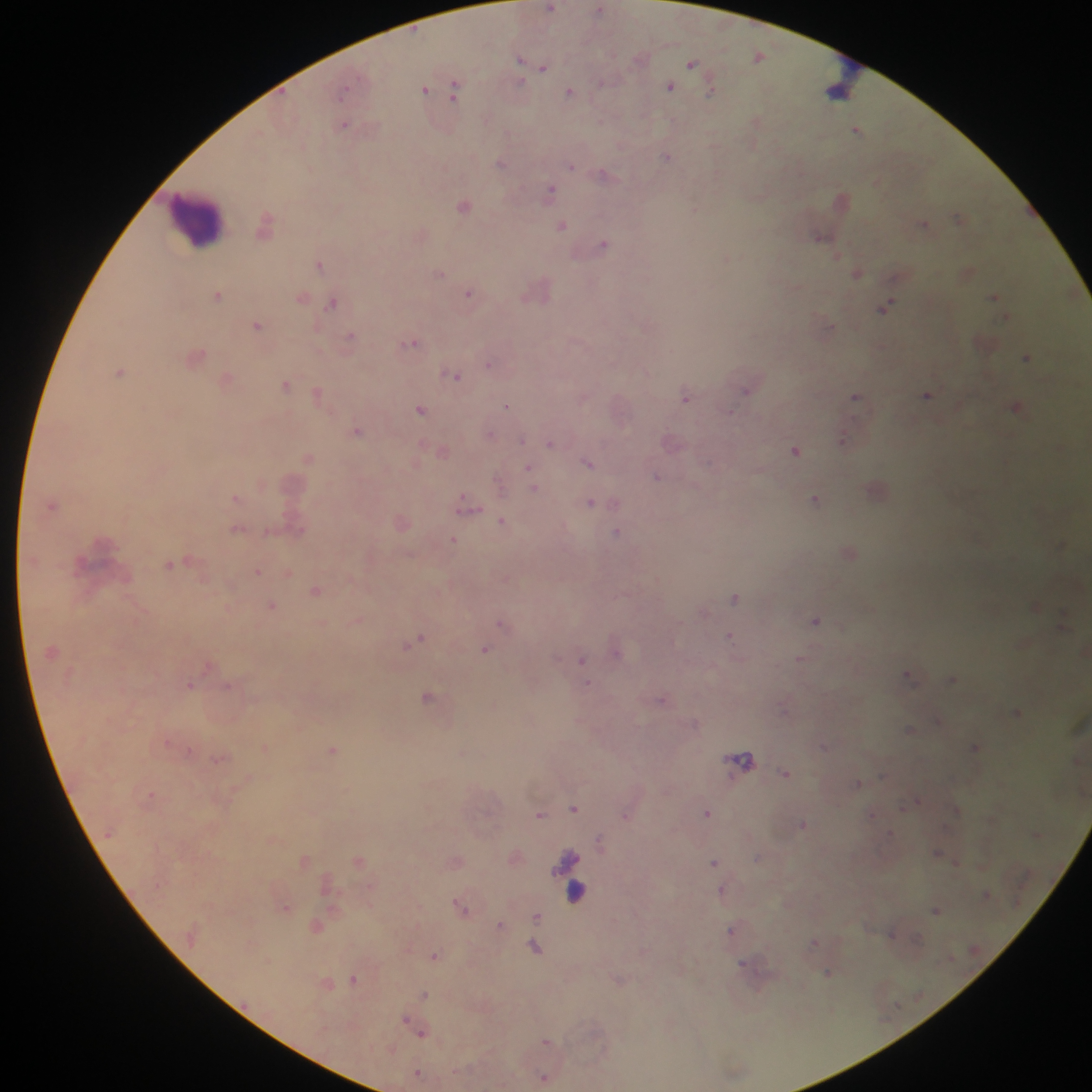
leukocyte locations = approximate centers as {x, y} in pixels: {847, 76}, {196, 222}, {583, 899}
image size = 1092×1092 pixels
field of view = single
Plasmodium parasite locations = approximate centers as {x, y} in pixels: {552, 8}, {758, 57}, {521, 58}, {692, 63}, {543, 69}, {520, 82}, {456, 86}, {671, 86}, {425, 89}, {712, 91}, {569, 93}, {602, 120}, {757, 122}, {344, 126}, {856, 131}, {668, 157}, {501, 164}, {571, 167}, {312, 172}, {604, 175}, {552, 192}, {844, 196}, {465, 207}, {695, 209}, {957, 216}, {267, 217}, {924, 223}, {562, 226}, {821, 236}, {604, 244}, {838, 255}, {727, 257}, {320, 264}, {857, 273}, {440, 274}, {469, 293}, {218, 295}, {302, 295}, {994, 296}, {332, 305}, {886, 306}, {256, 325}, {350, 338}, {414, 344}, {1027, 358}, {488, 364}, {120, 372}, {457, 376}, {285, 385}, {746, 389}, {317, 393}, {926, 395}, {857, 396}, {686, 399}, {508, 405}, {1015, 408}, {420, 411}, {358, 430}, {849, 431}, {522, 441}, {550, 444}, {423, 445}, {796, 451}, {589, 463}, {528, 467}, {656, 474}, {499, 486}, {535, 488}, {237, 499}, {815, 499}, {591, 501}, {50, 505}, {463, 508}, {502, 521}, {618, 532}, {454, 539}, {1058, 544}, {170, 565}, {258, 571}, {288, 571}, {317, 591}, {734, 599}, {272, 606}, {142, 611}, {357, 620}, {817, 620}, {501, 624}, {421, 636}, {730, 636}, {414, 641}, {407, 646}, {486, 648}, {799, 658}, {582, 659}, {209, 665}, {909, 675}, {952, 679}, {587, 683}, {230, 685}, {190, 686}, {428, 696}, {663, 700}, {938, 719}, {909, 729}, {168, 741}, {823, 745}, {976, 745}, {264, 747}, {333, 749}, {190, 750}, {218, 758}, {744, 762}, {787, 773}, {858, 782}, {152, 795}, {155, 795}, {919, 800}, {574, 809}, {957, 810}, {707, 813}, {872, 813}, {540, 814}, {626, 815}, {803, 823}, {599, 842}, {937, 852}, {305, 859}, {358, 860}, {715, 863}, {955, 863}, {720, 889}, {457, 903}, {286, 907}, {464, 908}, {935, 909}, {537, 917}, {500, 924}, {731, 931}, {891, 934}, {813, 942}, {535, 947}, {433, 955}, {269, 961}, {742, 962}, {827, 972}, {354, 978}, {425, 993}, {404, 1018}, {422, 1034}, {547, 1040}, {418, 1072}, {544, 1075}
country = Ghana
capture = mobile-phone photograph through a microscope
preparation = thick blood smear